Assess this cell for malaria.
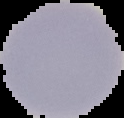

It is uninfected.

{
  "image_size": "124×118 pixels",
  "preparation": "thin blood film",
  "image_type": "cell region segmented out of the field of view; surrounding area masked to black"
}